Evaluate for malaria.
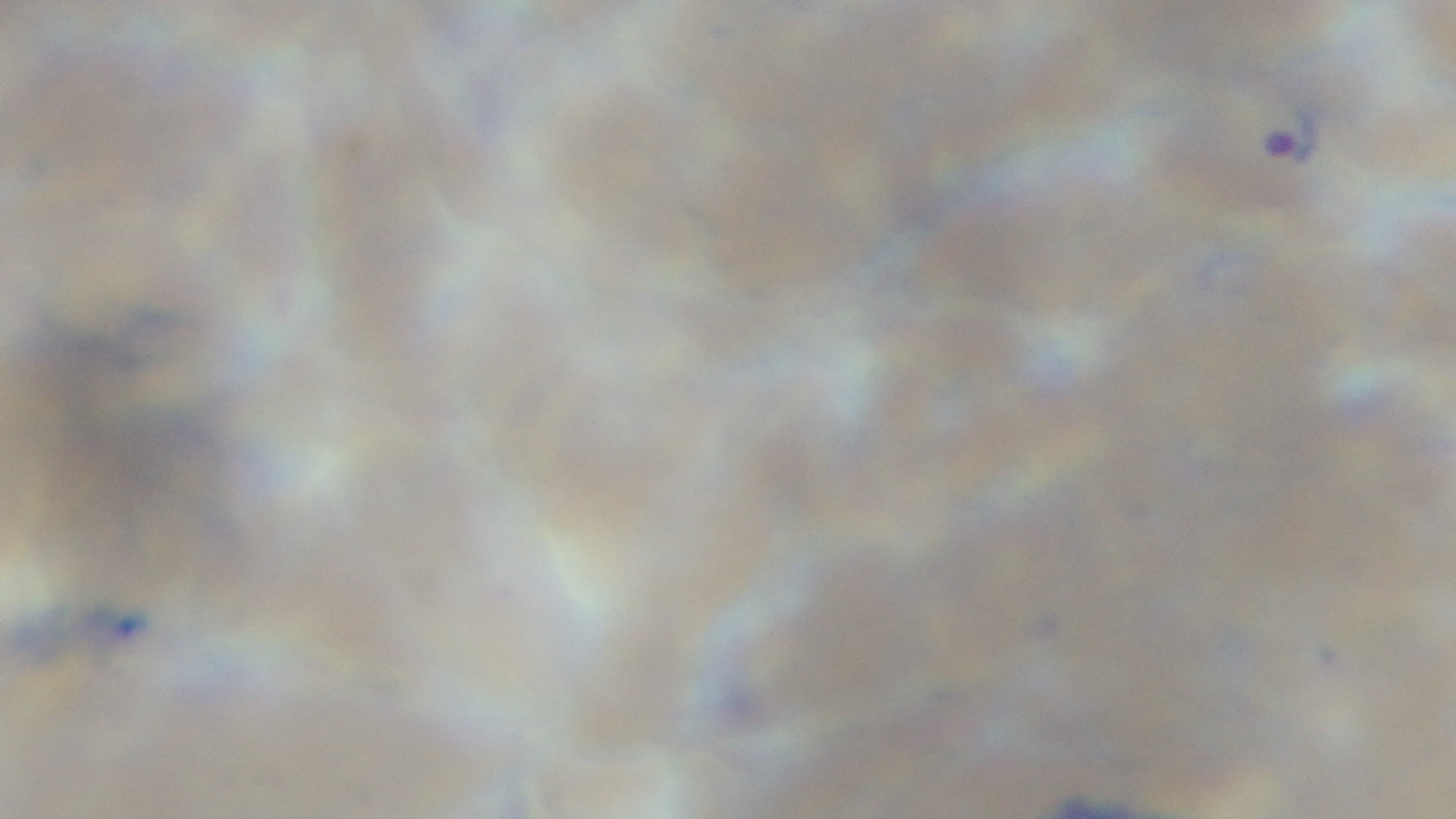

Infected.

Summary:
  - Modality: light microscopy
  - Stain: Giemsa
  - Capture: mounted 4K digital camera
  - Objective: 100x oil immersion
  - Preparation: thin
  - Field of view: single